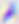

Toxoplasma gondii is seen. Micrograph. Captured at 400x magnification.